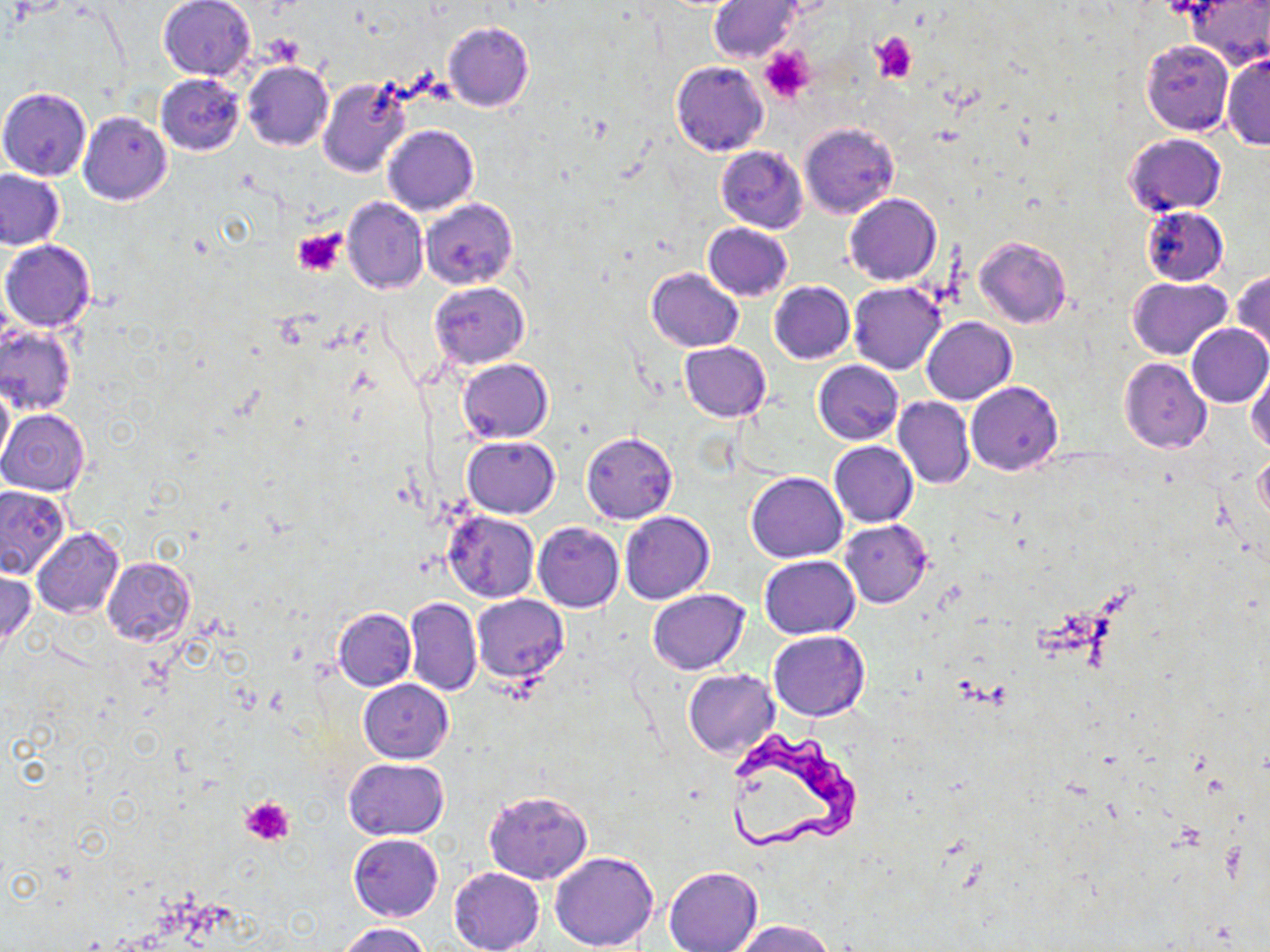
Approximate bounding boxes as (x1,y1)-(x2,y2) corner pairs in pixels. Uninfected red blood cell locations: (1185,0)-(1270,66), (157,1)-(257,80), (709,2)-(801,62), (442,21)-(535,112), (751,37)-(820,107), (1139,39)-(1235,136), (1221,51)-(1270,150), (670,60)-(769,156), (242,61)-(333,151), (155,74)-(246,154), (317,76)-(411,177), (0,87)-(91,181), (329,92)-(462,195), (78,111)-(172,205), (800,122)-(899,217), (383,125)-(479,215), (1124,132)-(1226,217), (715,145)-(809,232), (0,169)-(67,250), (845,193)-(940,285), (342,198)-(429,294), (421,199)-(516,289), (1140,205)-(1229,286), (702,222)-(793,300), (974,236)-(1071,328), (1,239)-(96,332), (645,268)-(743,351), (1232,270)-(1270,358), (1125,276)-(1233,360), (429,281)-(529,369), (769,281)-(856,363), (848,281)-(947,375), (922,317)-(1017,405), (1184,323)-(1270,409), (0,324)-(78,416), (679,342)-(771,421), (1119,357)-(1212,453), (457,358)-(553,442), (812,360)-(904,445), (1248,363)-(1270,453), (0,381)-(13,472), (965,381)-(1063,475), (893,397)-(975,489), (0,409)-(90,496), (581,432)-(678,524), (462,435)-(560,518), (819,439)-(923,605), (829,441)-(918,527), (1255,455)-(1270,525), (746,472)-(847,563), (0,485)-(70,579), (444,511)-(540,602), (619,511)-(714,604), (839,519)-(932,609), (533,522)-(624,613), (31,527)-(124,617), (33,540)-(189,633), (758,555)-(861,640), (102,556)-(195,647), (0,570)-(37,648), (646,589)-(749,675), (471,594)-(569,683), (404,596)-(482,696), (332,606)-(416,691), (769,630)-(871,721), (683,668)-(780,757), (359,679)-(454,763), (344,758)-(450,840), (482,789)-(593,885), (348,834)-(444,921), (550,851)-(659,951), (663,864)-(763,952), (448,867)-(545,952), (738,920)-(835,952), (336,921)-(431,952). Platelet locations: (871,34)-(916,82), (758,47)-(813,104), (293,226)-(346,276), (242,796)-(294,845). Trypanosoma brucei locations: (729,731)-(863,856). Slide-level diagnosis: Trypanosoma brucei. Captured at 1000x magnification. Optical microscopy. May-Grünwald-Giemsa stain. One field of a larger specimen. Image is 1270×952 pixels. Thin blood smear.